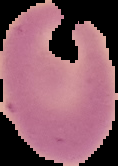
{
  "image_size": "118×166 pixels",
  "image_type": "cell region segmented out of the field of view; surrounding area masked to black",
  "preparation": "thin blood film",
  "malaria_status": "uninfected"
}